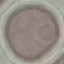
result = no malaria parasites seen
image type = automatically extracted cell patch, resized to 64 × 64 pixels
capture = smartphone through the microscope eyepiece
stain = Giemsa
preparation = thin blood smear